Assess this cell for malaria.
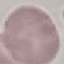
It is uninfected.

Giemsa-stained preparation. Automatically extracted cell patch, resized to 64 × 64 pixels. Thin blood film. Photographed with a smartphone camera at the microscope eyepiece.